Locate and identify every blood parasite.
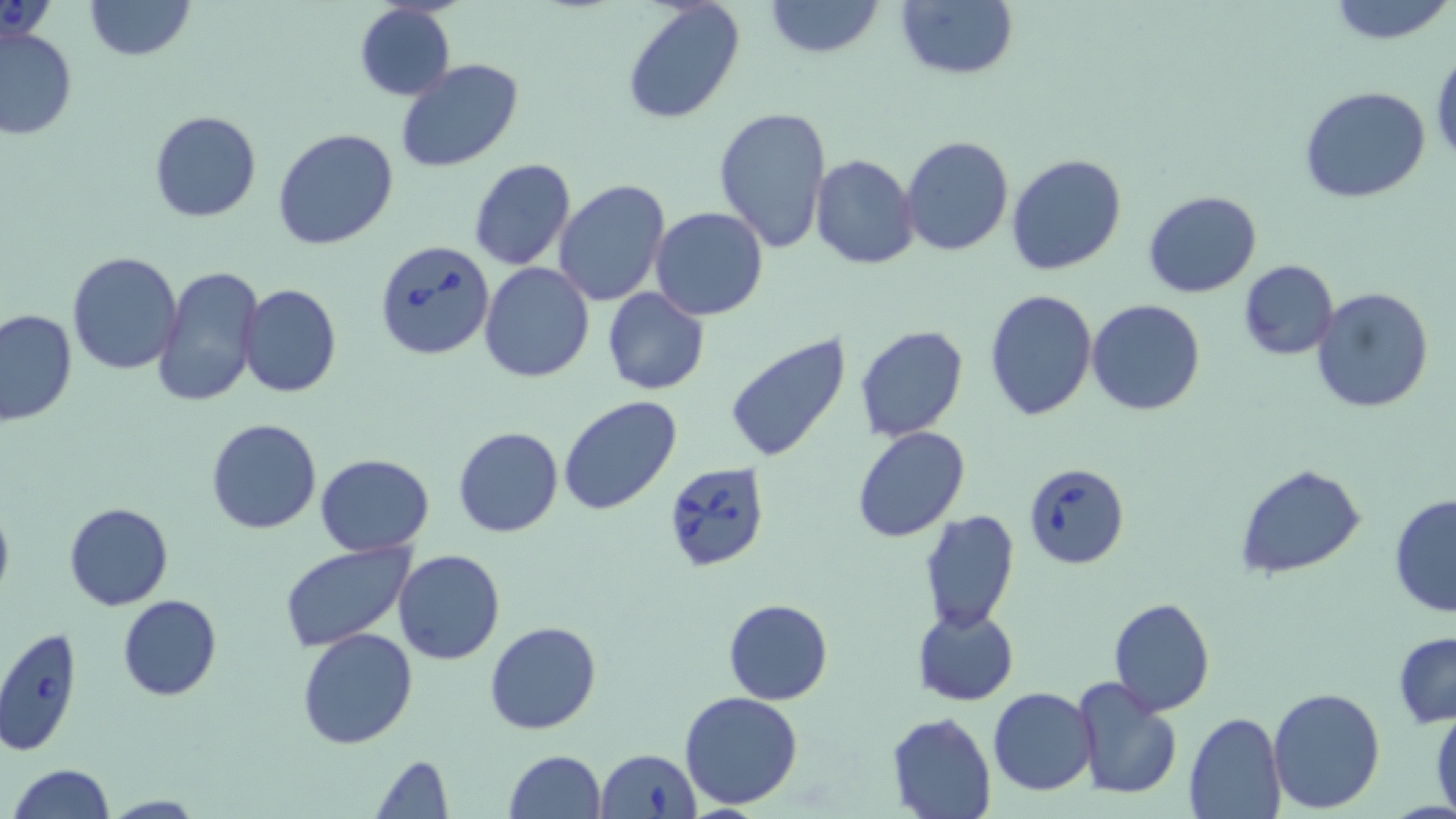
Approximate bounding boxes as (x1,y1)-(x2,y2) corner pairs in pixels.
Babesia divergens-infected red blood cells: (372,238)-(496,362), (663,461)-(772,571), (1024,461)-(1129,567), (0,627)-(81,758), (595,748)-(701,819).
No Plasmodium falciparum, Plasmodium ovale, Plasmodium malariae, Plasmodium vivax, or Trypanosoma brucei observed.

slide-level diagnosis = Babesia divergens
image size = 1456×819 pixels
magnification = 1000x
modality = light microscopy
uninfected red blood cell locations = approximate bounding boxes as (x1,y1)-(x2,y2) corner pairs in pixels: (81,0)-(196,60), (622,0)-(746,123), (765,0)-(884,58), (894,0)-(1018,81), (1327,0)-(1456,47), (354,3)-(455,102), (0,26)-(77,141), (1430,48)-(1456,168), (395,59)-(524,173), (1301,87)-(1431,204), (714,103)-(832,255), (148,110)-(262,223), (273,126)-(401,250), (900,137)-(1015,257), (810,154)-(920,271), (1005,154)-(1128,276), (468,158)-(577,271), (553,178)-(670,304), (1143,190)-(1263,298), (649,206)-(769,320), (66,250)-(184,376), (1238,259)-(1339,360), (480,263)-(596,383), (155,266)-(264,410), (239,284)-(342,397), (1311,286)-(1435,413), (603,289)-(710,395), (984,289)-(1098,421), (1087,300)-(1207,417), (0,309)-(77,427), (855,324)-(969,442), (725,333)-(852,464), (558,395)-(684,517), (206,418)-(321,534), (452,426)-(565,539), (851,426)-(969,541), (315,454)-(436,556), (1237,465)-(1367,580), (1388,493)-(1456,618), (0,498)-(15,605), (64,502)-(174,610), (918,509)-(1020,633), (281,542)-(416,651), (393,549)-(505,664), (117,594)-(221,701), (1107,597)-(1215,716), (723,598)-(833,706), (911,605)-(1020,706), (484,621)-(600,735), (297,628)-(419,749), (1393,630)-(1456,728), (1070,674)-(1183,800), (1267,686)-(1387,813), (988,687)-(1099,797), (680,691)-(803,810), (1431,706)-(1456,816), (887,711)-(996,819), (1183,711)-(1285,818), (503,750)-(607,819), (370,755)-(455,818), (6,764)-(116,819), (98,794)-(210,818)
field of view = single
preparation = thin blood smear
stain = May-Grünwald-Giemsa